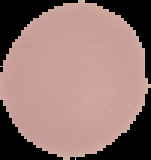
Summary:
  - Image size: 151×160 pixels
  - Malaria status: uninfected
  - Preparation: thin blood film
  - Image type: segmented cell region on a black background